Identify the parasite.
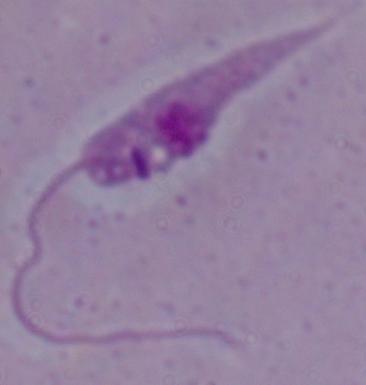
This is Leishmania.

Micrograph. Captured at 1000x magnification.